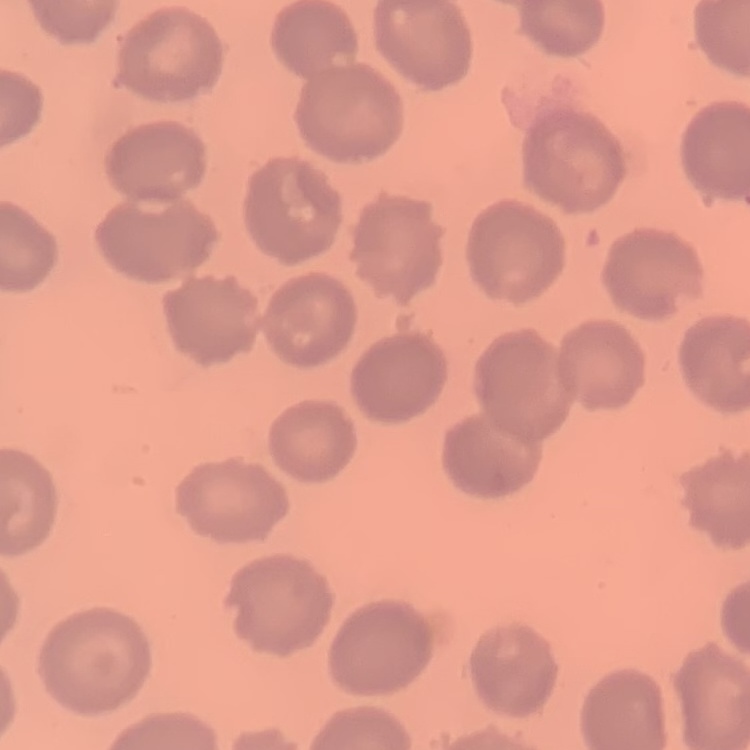

The red blood cells show no rouleaux formation. Stained with either Field's or Giemsa. Square crop of a larger photomicrograph. Thin blood smear.